Evaluate for Plasmodium parasites.
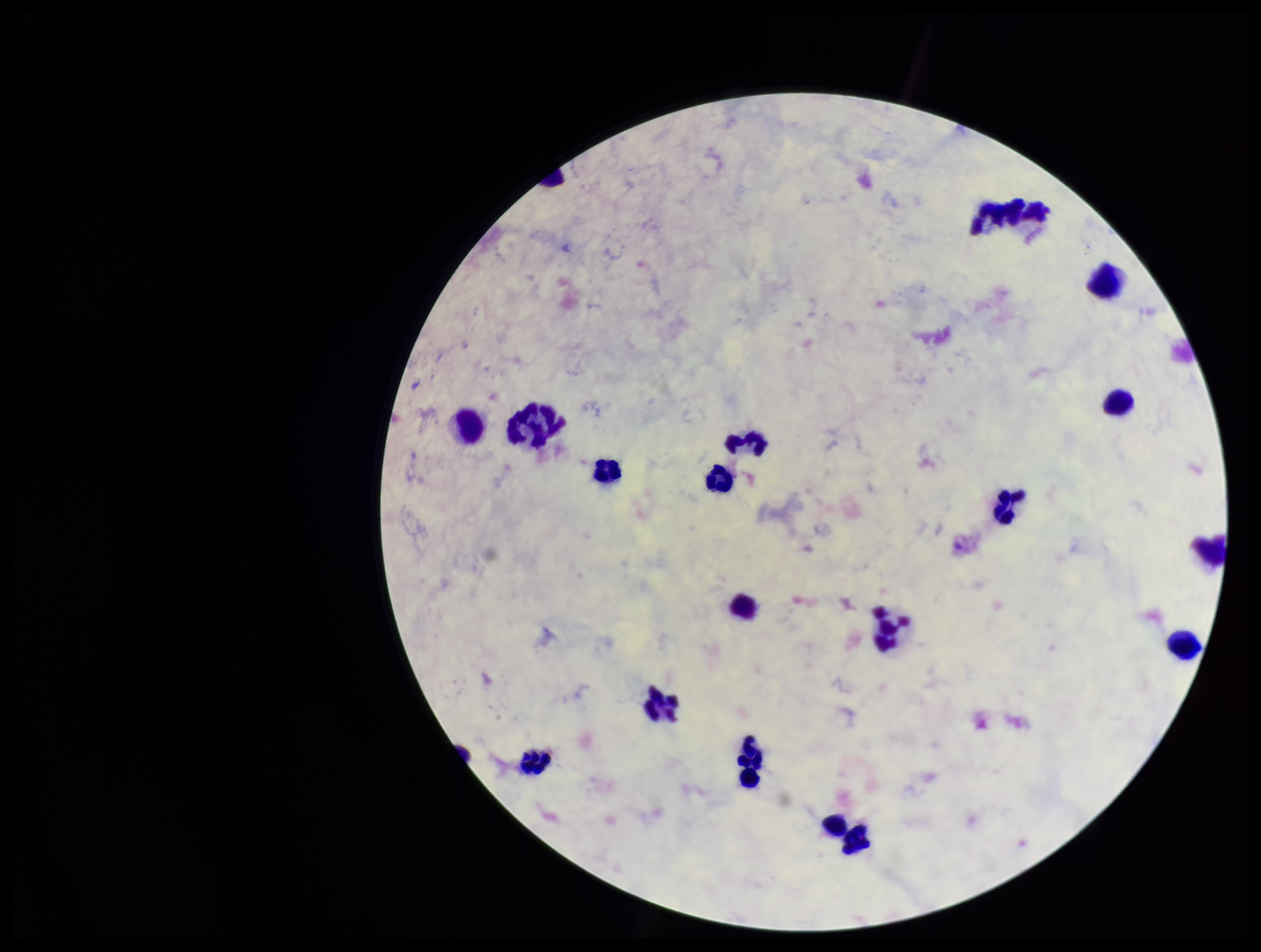
None seen.

Single field of view. Parasite count: 0. Patient malaria status: negative. Photographed through the microscope eyepiece with a smartphone camera. Preparation: thick blood smear. Stained with Giemsa. Image is 1261×952 pixels. Leukocyte count: 18.